Outline each blood parasite and name the species.
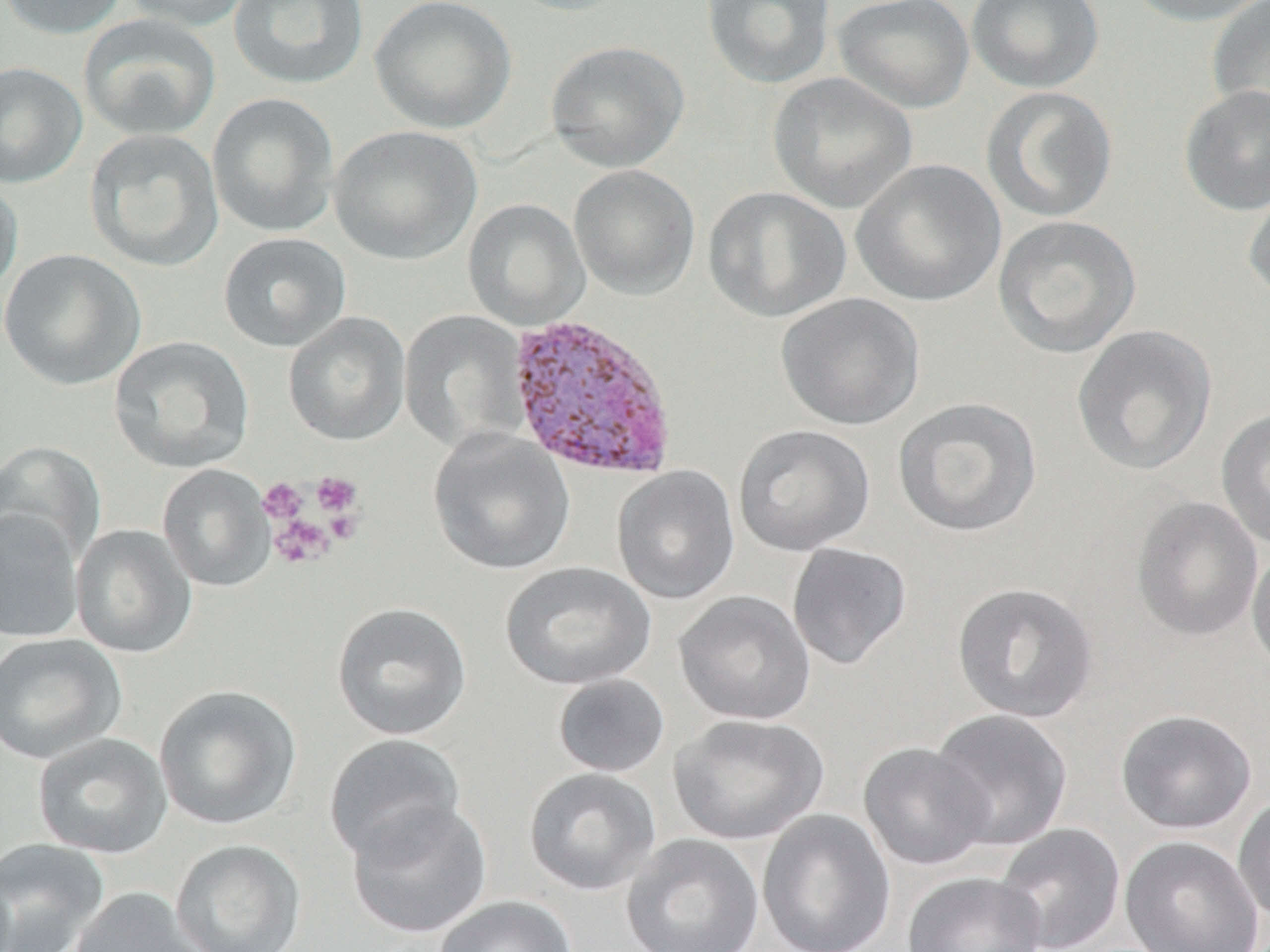
Approximate bounding boxes as named x1/y1/x2/y2 corners in pixels.
Plasmodium vivax-infected red blood cells: (x1=504, y1=312, x2=679, y2=482).
No Plasmodium falciparum, Plasmodium ovale, Plasmodium malariae, Babesia divergens, or Trypanosoma brucei observed.

slide-level diagnosis = Plasmodium vivax
field of view = one of a larger specimen
preparation = thin blood film
image size = 1270×952 pixels
modality = light microscopy
stain = May-Grünwald-Giemsa
magnification = 1000x
uninfected red blood cell locations = approximate bounding boxes as named x1/y1/x2/y2 corners in pixels: (x1=1, y1=0, x2=129, y2=40), (x1=120, y1=0, x2=254, y2=32), (x1=227, y1=0, x2=370, y2=90), (x1=369, y1=0, x2=517, y2=134), (x1=502, y1=0, x2=637, y2=16), (x1=700, y1=0, x2=836, y2=89), (x1=833, y1=0, x2=975, y2=114), (x1=966, y1=0, x2=1104, y2=93), (x1=1121, y1=0, x2=1270, y2=26), (x1=1206, y1=0, x2=1270, y2=129), (x1=78, y1=13, x2=222, y2=142), (x1=545, y1=40, x2=689, y2=172), (x1=0, y1=61, x2=87, y2=189), (x1=767, y1=72, x2=918, y2=214), (x1=1179, y1=85, x2=1270, y2=216), (x1=980, y1=86, x2=1118, y2=224), (x1=207, y1=92, x2=340, y2=237), (x1=328, y1=125, x2=482, y2=266), (x1=83, y1=128, x2=225, y2=272), (x1=851, y1=159, x2=1006, y2=307), (x1=568, y1=164, x2=700, y2=299), (x1=0, y1=175, x2=23, y2=299), (x1=1242, y1=179, x2=1270, y2=306), (x1=703, y1=186, x2=851, y2=322), (x1=463, y1=198, x2=590, y2=330), (x1=993, y1=214, x2=1142, y2=360), (x1=218, y1=233, x2=351, y2=352), (x1=0, y1=249, x2=145, y2=391), (x1=776, y1=293, x2=925, y2=430), (x1=400, y1=310, x2=531, y2=453), (x1=283, y1=312, x2=411, y2=446), (x1=1071, y1=324, x2=1218, y2=476), (x1=109, y1=336, x2=255, y2=473), (x1=892, y1=396, x2=1043, y2=538), (x1=1216, y1=406, x2=1270, y2=552), (x1=733, y1=423, x2=875, y2=557), (x1=428, y1=429, x2=576, y2=576), (x1=0, y1=441, x2=107, y2=567), (x1=157, y1=464, x2=275, y2=592), (x1=612, y1=465, x2=741, y2=605), (x1=1130, y1=495, x2=1264, y2=642), (x1=0, y1=509, x2=84, y2=643), (x1=70, y1=525, x2=196, y2=658), (x1=786, y1=542, x2=913, y2=670), (x1=1247, y1=544, x2=1270, y2=680), (x1=500, y1=561, x2=656, y2=691), (x1=951, y1=582, x2=1099, y2=723), (x1=672, y1=590, x2=816, y2=726), (x1=332, y1=602, x2=472, y2=740), (x1=0, y1=633, x2=127, y2=764), (x1=551, y1=673, x2=670, y2=777), (x1=154, y1=684, x2=301, y2=830), (x1=930, y1=708, x2=1073, y2=852), (x1=1115, y1=709, x2=1257, y2=834), (x1=668, y1=713, x2=829, y2=845), (x1=33, y1=732, x2=173, y2=859), (x1=324, y1=734, x2=465, y2=863), (x1=859, y1=742, x2=993, y2=871), (x1=524, y1=767, x2=661, y2=895), (x1=1233, y1=793, x2=1270, y2=926), (x1=345, y1=799, x2=492, y2=939), (x1=757, y1=809, x2=896, y2=952), (x1=993, y1=823, x2=1125, y2=952), (x1=621, y1=833, x2=764, y2=952), (x1=1119, y1=835, x2=1264, y2=952), (x1=0, y1=837, x2=111, y2=952), (x1=170, y1=839, x2=307, y2=952), (x1=902, y1=871, x2=1046, y2=952), (x1=69, y1=887, x2=210, y2=951), (x1=433, y1=895, x2=577, y2=952)
platelet locations = approximate bounding boxes as named x1/y1/x2/y2 corners in pixels: (x1=311, y1=471, x2=363, y2=518), (x1=258, y1=477, x2=308, y2=525), (x1=268, y1=514, x2=336, y2=569)